Report the malaria status of this cell.
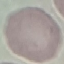
It is uninfected.

Thin blood smear. Photographed with a smartphone camera at the microscope eyepiece. Giemsa-stained preparation. Automatically extracted cell patch, resized to 64 × 64 pixels.